Comment on the background quality.
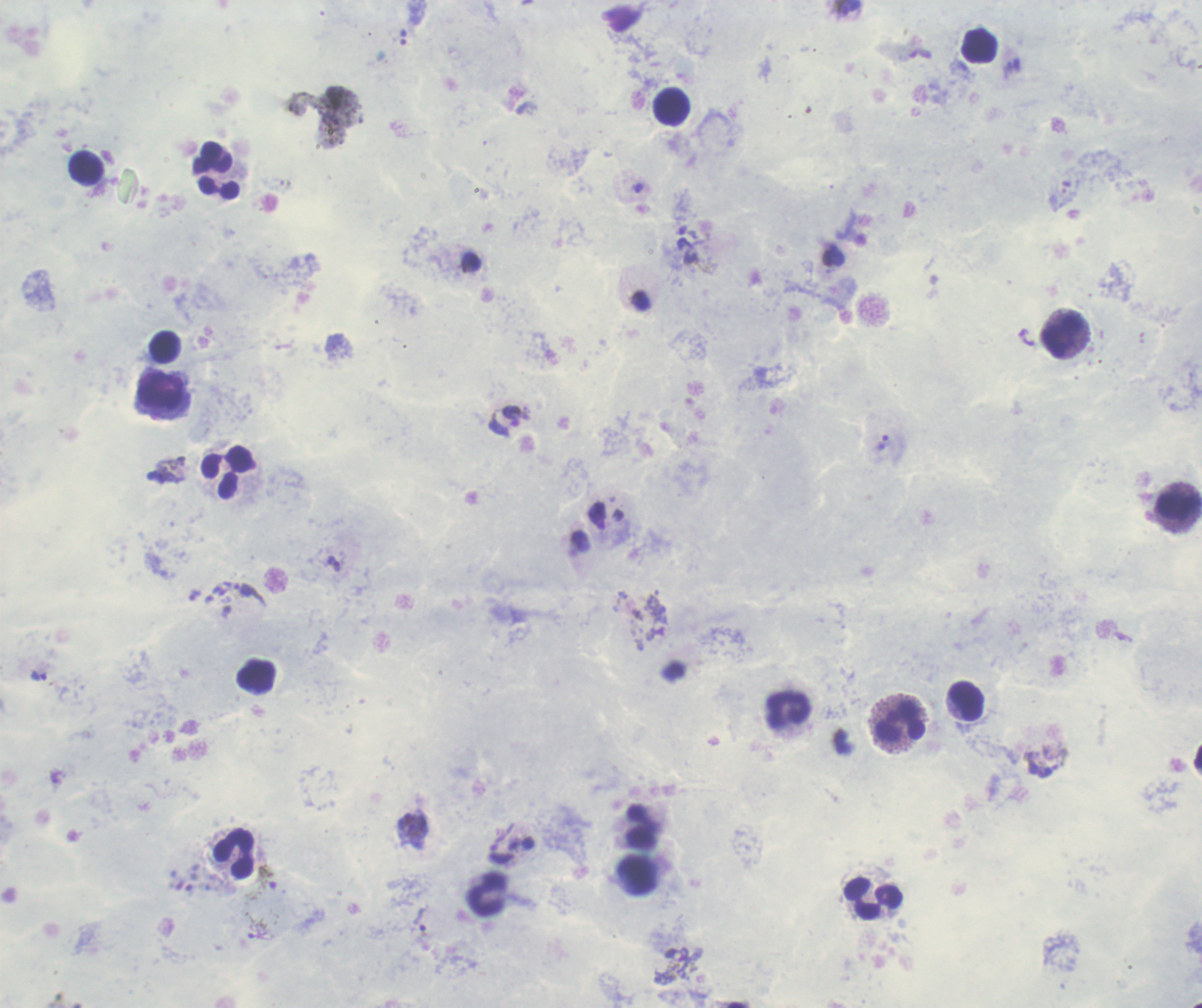
Unsatisfactory.

life_cycle_stages_observed: trophozoite, gametocyte
image_size: 1202×1008 pixels
magnification: 100x
field_of_view: one from this slide
leukocyte_locations: 'approximate object centers, in pixels from the top-left corner: (x=671, y=106), (x=212, y=157), (x=87, y=168), (x=219, y=188), (x=1063, y=336), (x=163, y=347), (x=162, y=390), (x=229, y=472), (x=1178, y=505), (x=255, y=676), (x=965, y=701), (x=790, y=710), (x=902, y=723), (x=642, y=826), (x=234, y=854), (x=487, y=895), (x=872, y=899)'
context: previously used in an actual diagnosis
coloration_quality: good
result: malaria parasites detected
stain: Romanowsky
preparation: thick blood smear
trophozoite_locations: 'approximate object centers, in pixels from the top-left corner: (x=638, y=188), (x=686, y=237), (x=512, y=415), (x=882, y=442), (x=334, y=563), (x=1042, y=764), (x=420, y=919), (x=681, y=962)'
gametocyte_locations: 'approximate object centers, in pixels from the top-left corner: (x=266, y=880)'